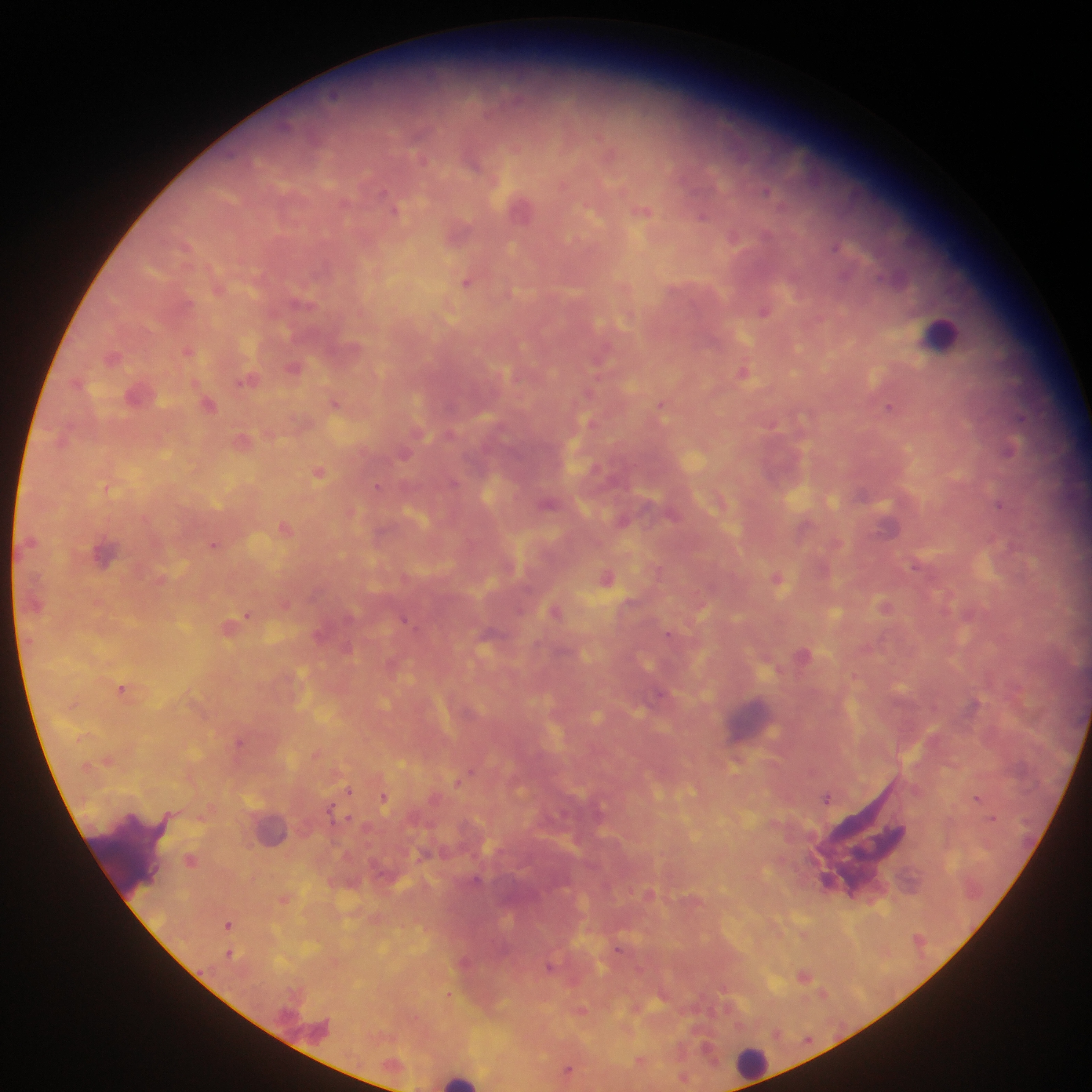
country = Ghana
capture = mobile-phone photograph through a microscope
malaria parasite locations = approximate centers as (x, y) in pixels: (334, 96), (285, 125), (422, 159), (473, 162), (766, 191), (394, 208), (643, 211), (702, 216), (766, 235), (733, 236), (186, 245), (834, 248), (844, 275), (467, 282), (764, 311), (188, 350), (113, 358), (294, 367), (743, 372), (246, 380), (334, 402), (661, 404), (208, 405), (888, 406), (1021, 417), (1008, 449), (404, 454), (319, 472), (453, 482), (376, 486), (548, 504), (1000, 504), (623, 521), (285, 526), (214, 545), (914, 565), (607, 577), (777, 578), (885, 606), (555, 611), (246, 615), (404, 620), (668, 634), (122, 688), (660, 693), (239, 742), (469, 772), (348, 790), (826, 797), (383, 798), (977, 798), (330, 811), (348, 818), (992, 818), (191, 860), (476, 879), (827, 880), (228, 925), (617, 948), (230, 953), (550, 965), (804, 975), (568, 1070)
image size = 1092×1092 pixels
leukocyte locations = approximate centers as (x, y) in pixels: (942, 333), (753, 719), (120, 850), (751, 1061), (460, 1077)
field of view = single
preparation = thick blood smear